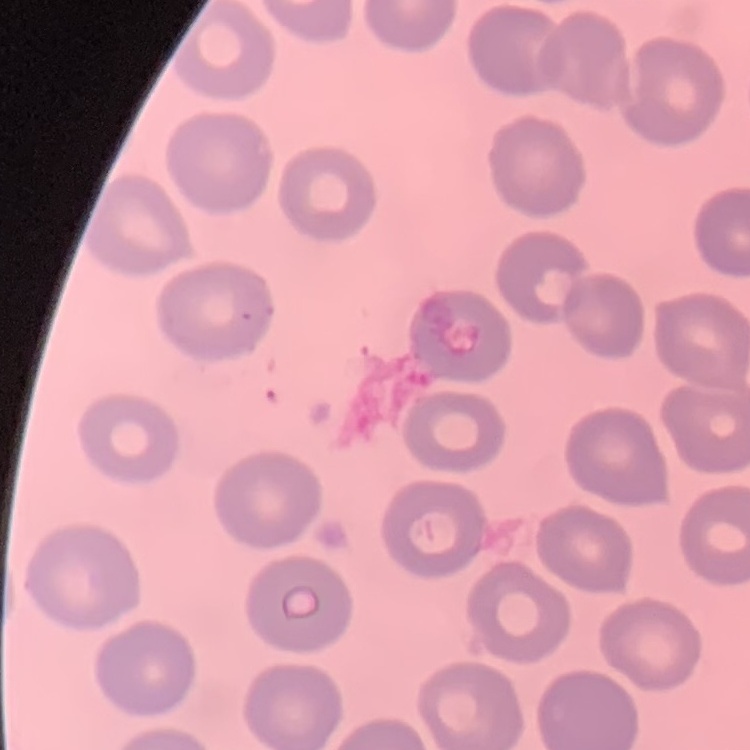

{
  "erythrocyte_morphology": "no rouleaux formation",
  "stain": "Field's or Giemsa",
  "image_type": "one tile cut from a larger photomicrograph",
  "preparation": "thin blood film"
}